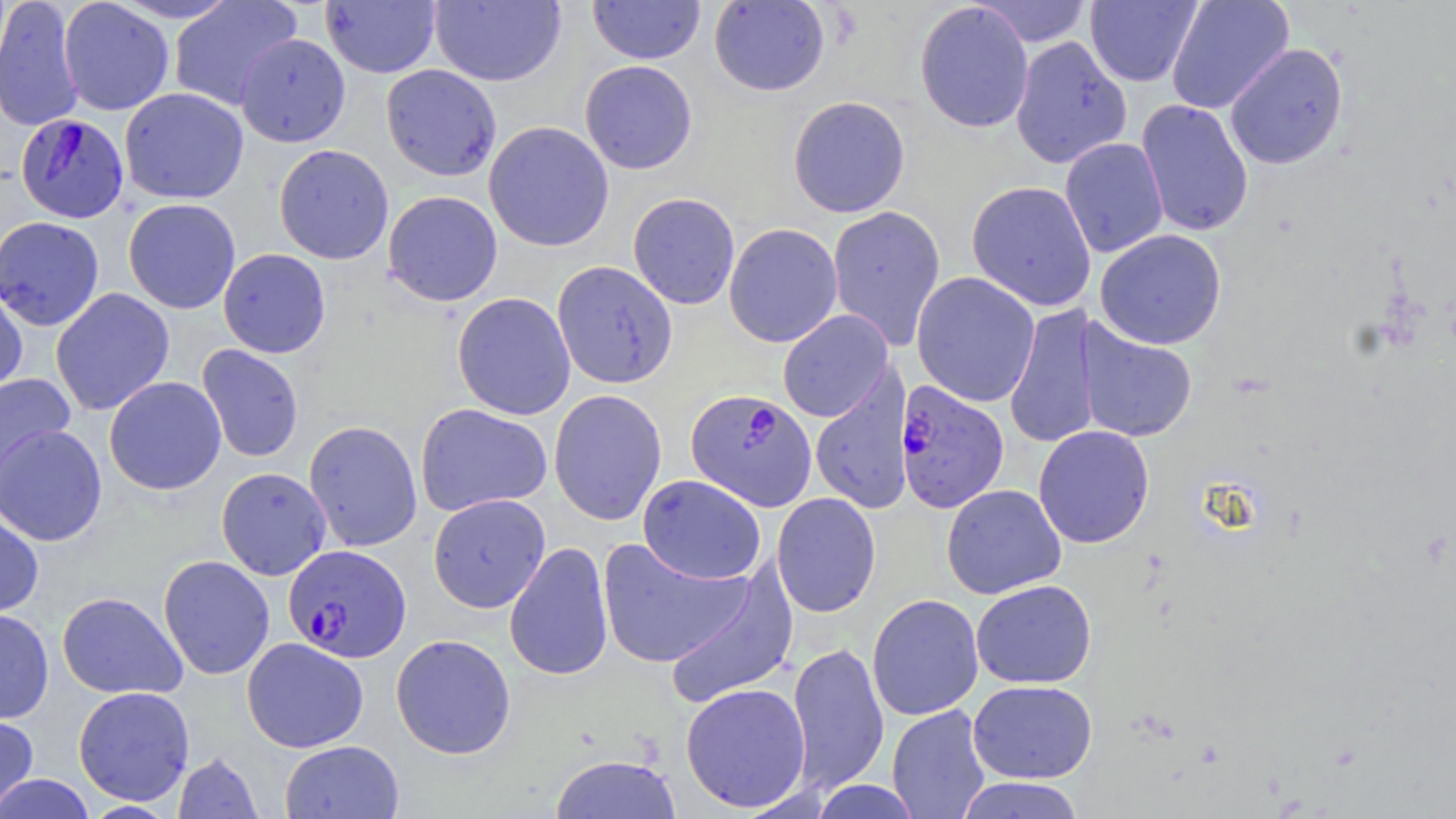
slide-level diagnosis = Plasmodium falciparum
modality = light microscopy
image size = 1456×819 pixels
magnification = 1000x
Plasmodium falciparum-infected red blood cell locations = approximate bounding boxes as (x1, y1, x2, y2) in pixels: (14, 113, 129, 224), (894, 380, 1010, 513), (685, 389, 817, 510), (283, 544, 411, 662)
stain = May-Grünwald-Giemsa
uninfected red blood cell locations = approximate bounding boxes as (x1, y1, x2, y2) in pixels: (0, 0, 84, 133), (430, 0, 566, 87), (588, 0, 705, 64), (971, 0, 1094, 47), (1085, 0, 1202, 87), (1166, 0, 1293, 114), (58, 1, 174, 116), (168, 1, 302, 111), (321, 1, 441, 78), (708, 1, 830, 96), (915, 1, 1034, 133), (235, 33, 351, 147), (1010, 36, 1132, 169), (1225, 43, 1348, 169), (580, 60, 697, 174), (382, 64, 501, 181), (119, 87, 248, 204), (788, 95, 910, 217), (1135, 100, 1254, 237), (484, 121, 614, 251), (1059, 137, 1169, 258), (274, 144, 394, 265), (967, 181, 1096, 311), (382, 190, 503, 306), (628, 192, 740, 309), (123, 198, 241, 314), (827, 205, 945, 350), (1, 216, 105, 331), (724, 222, 843, 347), (1095, 229, 1227, 349), (218, 248, 331, 358), (552, 260, 677, 389), (911, 272, 1040, 407), (0, 285, 28, 398), (50, 287, 175, 416), (452, 292, 576, 420), (1004, 302, 1100, 450), (777, 310, 893, 422), (1077, 318, 1198, 443), (197, 344, 304, 462), (0, 370, 76, 498), (810, 370, 914, 516), (104, 376, 227, 495), (548, 389, 668, 526), (415, 403, 552, 516), (303, 420, 423, 552), (0, 423, 107, 547), (1033, 425, 1155, 548), (216, 467, 332, 580), (638, 474, 767, 584), (941, 483, 1066, 599), (771, 492, 882, 618), (427, 493, 550, 613), (0, 511, 44, 618), (597, 537, 751, 669), (504, 541, 613, 681), (158, 555, 275, 680), (664, 565, 798, 710), (971, 579, 1096, 689), (56, 591, 187, 699), (867, 593, 984, 721), (0, 608, 54, 724), (391, 633, 516, 759), (241, 637, 368, 753), (787, 641, 889, 793), (968, 679, 1097, 783), (680, 682, 812, 812), (73, 686, 195, 805), (887, 705, 990, 819), (0, 712, 39, 818), (280, 739, 404, 818), (172, 752, 264, 818), (548, 753, 682, 819), (1, 774, 95, 818), (953, 777, 1086, 819), (809, 779, 925, 818)
field of view = one of a larger specimen
preparation = thin blood film